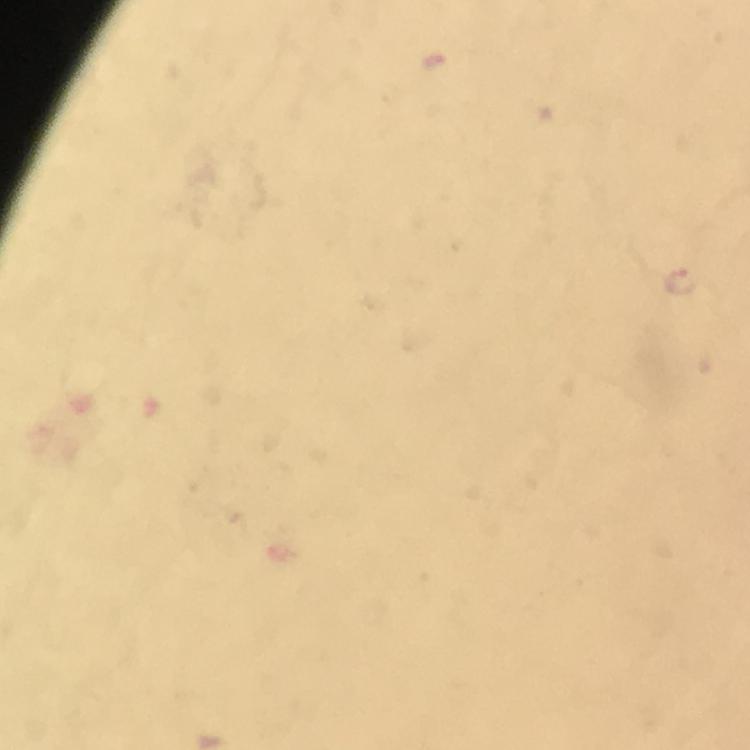
Approximate centers as {x, y} in pixels. Malaria parasite locations: {682, 281}. Photographed with a smartphone mounted on the microscope. Image is 750×750 pixels. Immersion oil applied. Thick blood film. At 100x magnification. From a malaria diagnostic workup. Cropped region of a single field of view. Giemsa stain.